Outline each white blood cell.
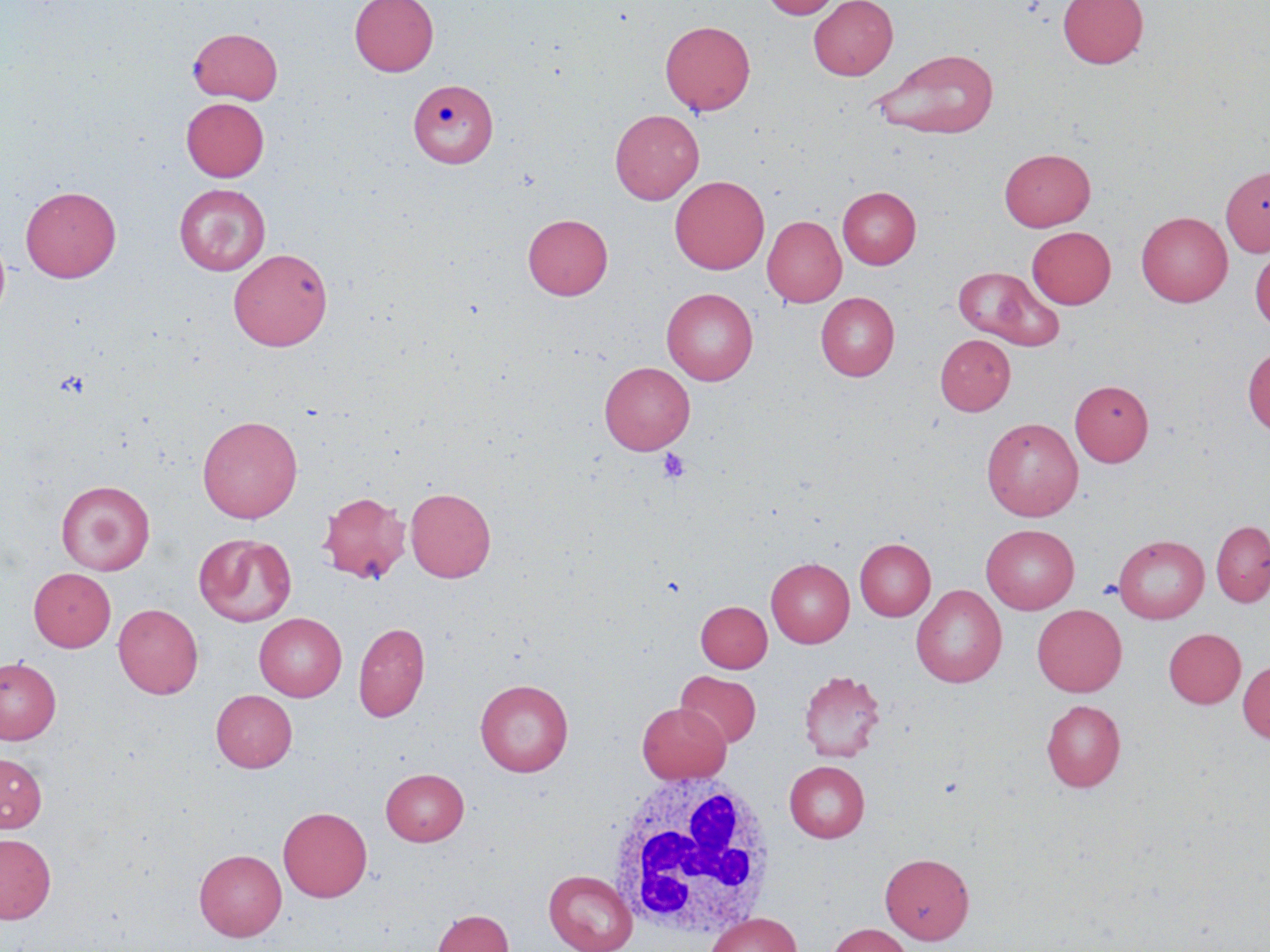
Approximate bounding boxes as [x1, y1, x2, y2] in pixels.
White blood cells: [605, 769, 778, 940].

Platelet locations: [657, 448, 690, 484]. Uninfected red blood cell locations: [349, 0, 438, 76], [760, 0, 841, 18], [808, 0, 898, 80], [1058, 0, 1148, 69], [660, 20, 755, 116], [188, 27, 283, 104], [873, 48, 1000, 139], [409, 79, 498, 168], [181, 98, 269, 181], [610, 109, 704, 204], [999, 148, 1095, 231], [1220, 165, 1270, 256], [670, 175, 769, 274], [174, 184, 270, 275], [20, 185, 121, 282], [837, 186, 921, 268], [1136, 211, 1233, 306], [523, 214, 612, 300], [762, 215, 846, 307], [1027, 226, 1115, 308], [0, 230, 11, 324], [1250, 246, 1270, 331], [229, 248, 333, 351], [953, 266, 1063, 350], [662, 288, 758, 385], [816, 292, 899, 381], [935, 334, 1015, 416], [1243, 345, 1270, 436], [600, 362, 694, 454], [1070, 380, 1154, 466], [197, 415, 303, 523], [982, 418, 1083, 521], [56, 480, 155, 575], [405, 487, 496, 582], [318, 491, 410, 584], [1210, 520, 1270, 608], [981, 524, 1079, 613], [195, 534, 296, 626], [1113, 534, 1209, 623], [854, 538, 935, 620], [766, 558, 854, 647], [28, 568, 116, 652], [911, 585, 1006, 688], [696, 601, 772, 672], [113, 603, 203, 698], [1032, 604, 1126, 696], [254, 613, 346, 701], [353, 621, 430, 722], [1163, 628, 1246, 708], [0, 657, 61, 744], [1237, 660, 1270, 743], [799, 670, 886, 763], [676, 671, 761, 748], [475, 678, 573, 777], [211, 690, 297, 771], [1041, 700, 1125, 791], [636, 702, 731, 783], [0, 753, 47, 832], [784, 761, 870, 842], [381, 768, 469, 845], [278, 807, 372, 902], [0, 833, 56, 923], [194, 849, 286, 941], [880, 852, 974, 943], [543, 869, 637, 952], [432, 909, 513, 952], [704, 913, 802, 952], [826, 923, 912, 952]. Slide-level diagnosis: no evidence of blood parasites. Image is 1270×952 pixels. Captured at 1000x magnification. One field of a larger specimen. Light microscopy. May-Grünwald-Giemsa-stained preparation. Thin blood film.